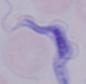

Summary:
  - Identification: trypanosome
  - Modality: photomicrograph
  - Magnification: 1000x